Locate every uninfected red blood cell.
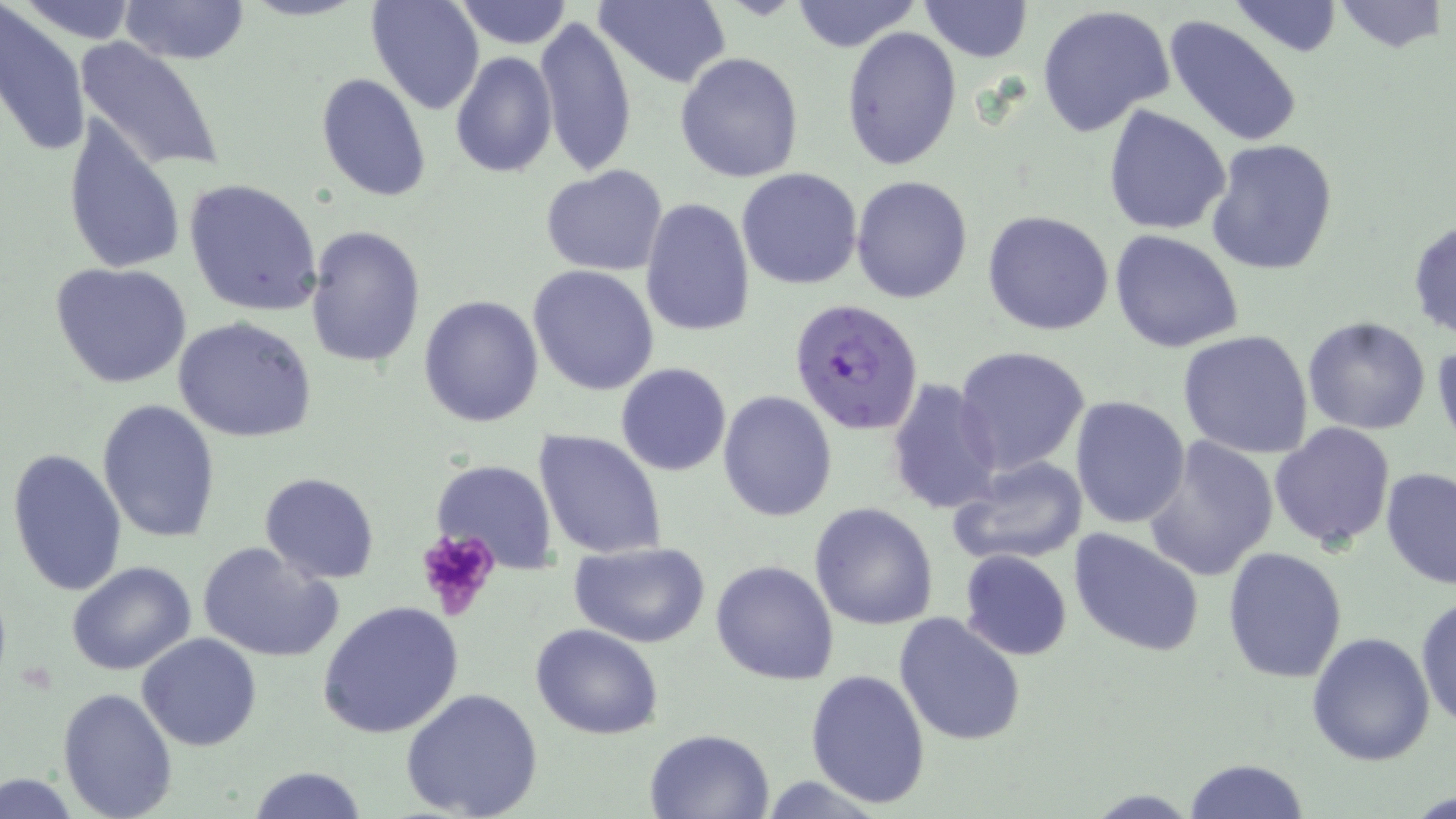

Approximate bounding boxes as [x1, y1, x2, y2] in pixels.
Uninfected red blood cells: [15, 0, 142, 44], [118, 0, 252, 65], [365, 0, 484, 115], [454, 0, 574, 48], [596, 0, 732, 89], [789, 0, 923, 53], [920, 0, 1032, 63], [1226, 0, 1344, 58], [1331, 0, 1449, 55], [0, 5, 90, 162], [1037, 5, 1174, 140], [1162, 14, 1304, 150], [535, 15, 637, 178], [841, 26, 963, 171], [75, 37, 227, 175], [675, 51, 805, 183], [450, 52, 557, 176], [316, 73, 431, 201], [1103, 104, 1233, 235], [62, 112, 186, 278], [1204, 138, 1340, 275], [541, 165, 669, 275], [735, 168, 863, 290], [851, 174, 973, 304], [183, 177, 325, 316], [640, 198, 755, 338], [981, 210, 1115, 335], [1408, 219, 1455, 340], [303, 224, 427, 369], [1109, 230, 1244, 352], [51, 261, 193, 389], [527, 264, 660, 395], [418, 295, 545, 426], [172, 315, 317, 443], [1301, 315, 1432, 434], [1176, 330, 1315, 461], [1432, 333, 1456, 450], [954, 345, 1091, 474], [615, 362, 732, 477], [884, 379, 1002, 514], [718, 390, 837, 522], [1070, 395, 1192, 529], [97, 398, 222, 544], [1269, 421, 1395, 552], [533, 429, 667, 560], [1141, 436, 1279, 582], [6, 447, 129, 597], [944, 453, 1092, 569], [430, 458, 557, 573], [1380, 466, 1456, 592], [259, 471, 380, 583], [238, 475, 370, 665], [809, 502, 938, 629], [1067, 527, 1207, 660], [198, 541, 344, 662], [568, 541, 711, 646], [1222, 548, 1348, 683], [959, 550, 1072, 660], [68, 560, 196, 676], [710, 560, 838, 685], [1415, 592, 1456, 733], [318, 601, 464, 740], [895, 612, 1026, 744], [532, 622, 662, 739], [1305, 630, 1436, 766], [139, 633, 261, 751], [804, 669, 931, 808], [58, 686, 178, 817], [399, 687, 545, 819], [645, 728, 773, 818], [1183, 758, 1310, 818], [247, 765, 366, 819], [0, 774, 81, 816].

Plasmodium falciparum-infected red blood cell locations: [789, 297, 924, 435]. Platelet locations: [412, 528, 501, 618]. Slide-level diagnosis: Plasmodium falciparum. Optical microscopy. One field of a larger specimen. 1000x magnification. Image is 1456×819 pixels. May-Grünwald-Giemsa stain. Thin blood film.